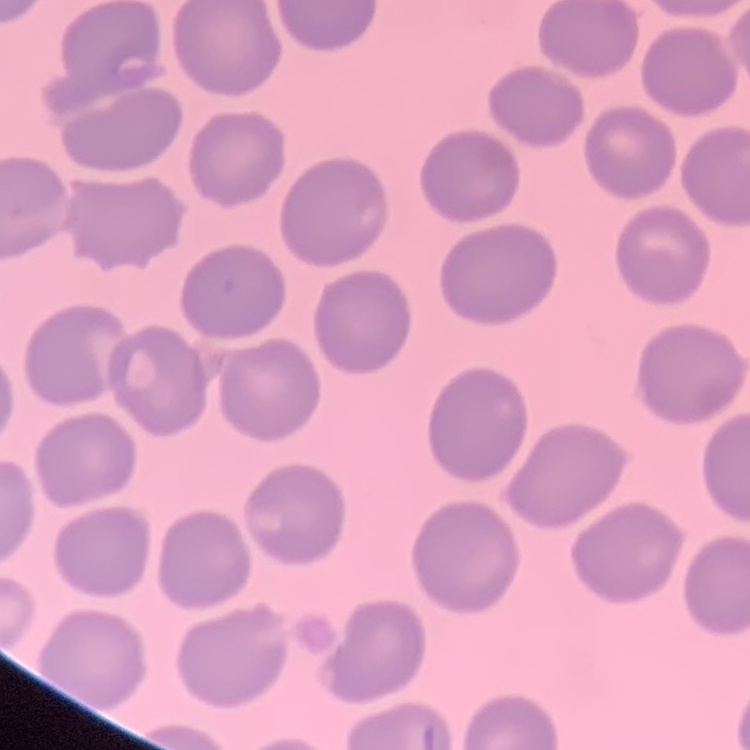
The erythrocytes show no rouleaux formation. Square crop of a larger photomicrograph. Stained with either Field's or Giemsa. Thin blood film.